Comment on the morphology of the red blood cells.
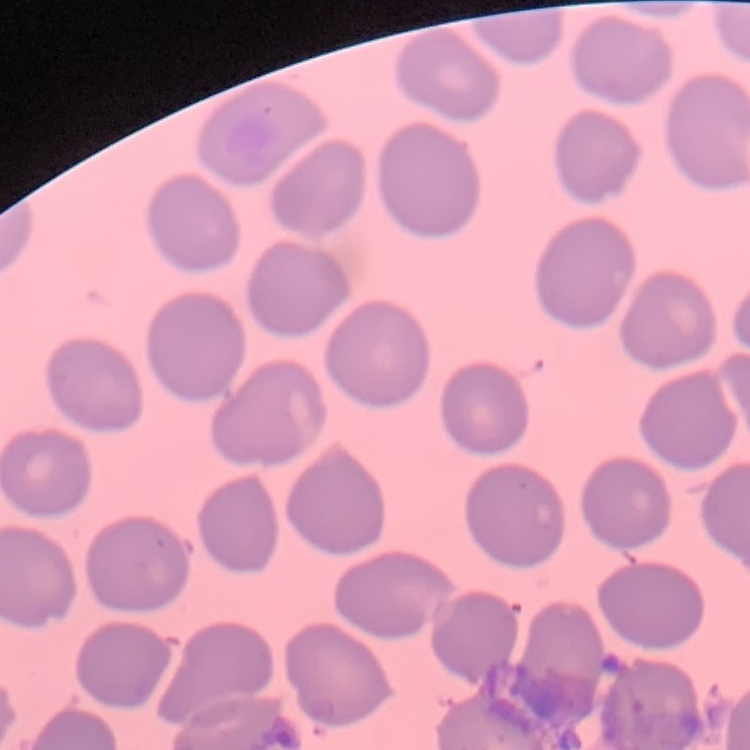

They show no rouleaux formation.

One tile cut from a larger photomicrograph. Stained with either Field's or Giemsa. Thin blood film.